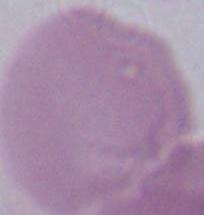
Summary:
  - Identification: erythrocyte
  - Magnification: 1000x
  - Modality: photomicrograph